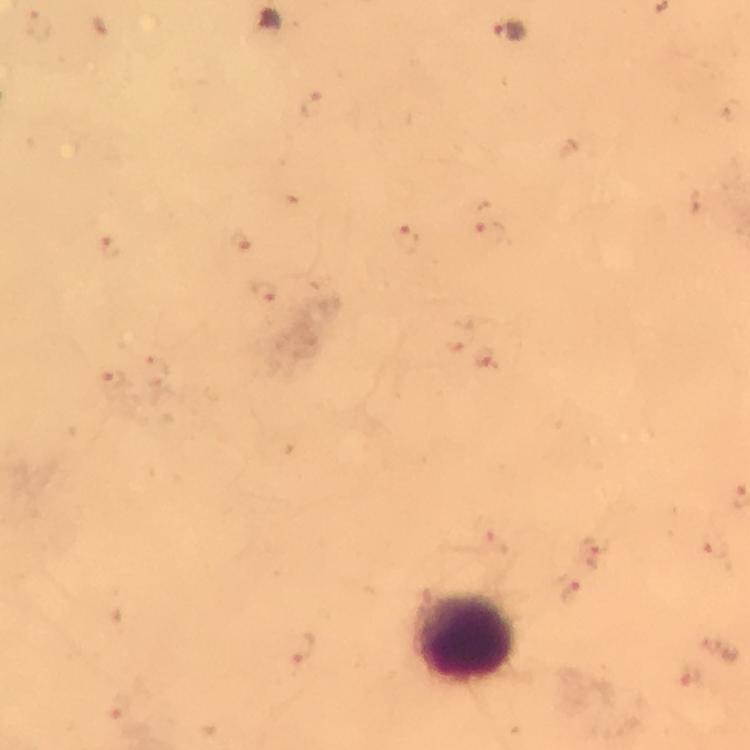
Approximate centers as [x, y] in pixels.
Summary:
  - Plasmodium parasite locations: [270, 18], [511, 30]
  - Leukocyte locations: [465, 634]
  - Image size: 750×750 pixels
  - Stain: Giemsa
  - Preparation: thick blood smear
  - Immersion oil: used
  - Cropped from: one field of view
  - Magnification: 100x
  - Context: from a malaria diagnostic workup
  - Capture: smartphone mounted on the microscope